Report the malaria status of this cell.
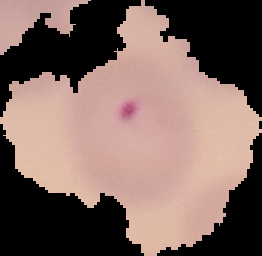

Parasitized.

From a thin blood film. Image is 262×256 pixels. The area outside the segmented cell region is set to black.